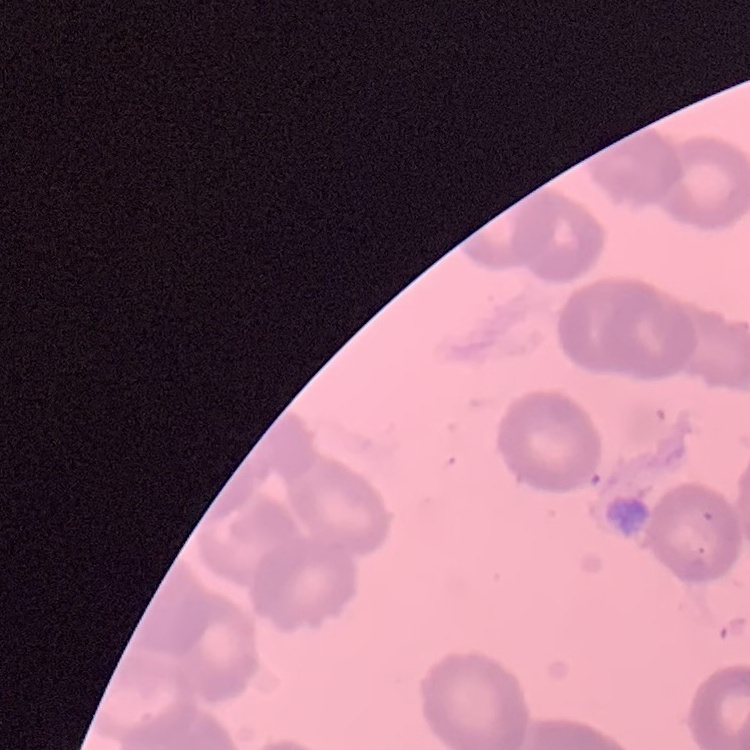
Summary:
  - Erythrocyte morphology: rouleaux formation
  - Image type: one tile cut from a larger photomicrograph
  - Stain: Field's or Giemsa
  - Preparation: thin blood film